Classify this cell by malaria status.
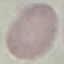
Uninfected.

Thin blood film. Giemsa stain. Photographed with a smartphone camera at the microscope eyepiece. Automatically extracted cell patch, resized to 64 × 64 pixels.